State which parasite is depicted.
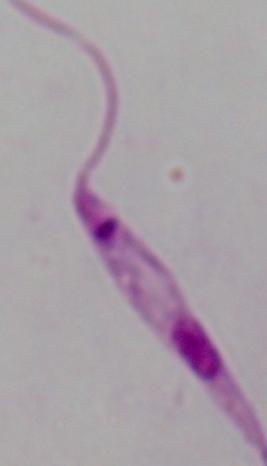
This is Leishmania.

Summary:
  - Modality: micrograph
  - Magnification: 1000x